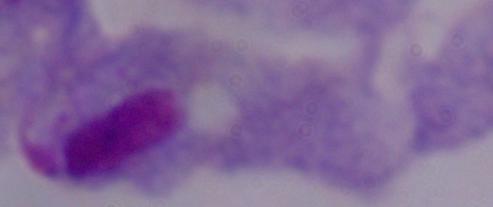
{
  "magnification": "1000x",
  "modality": "photomicrograph",
  "identification": "trichomonad"
}